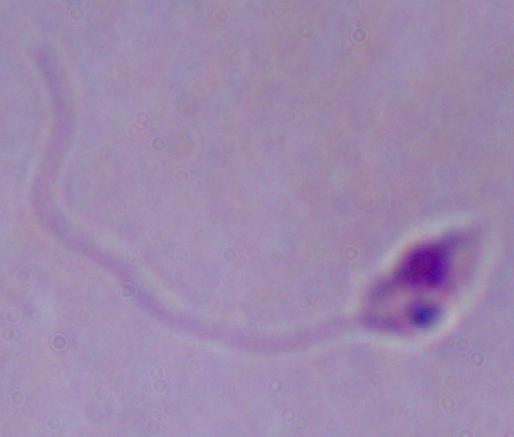

{
  "modality": "micrograph",
  "identification": "Leishmania",
  "magnification": "1000x"
}